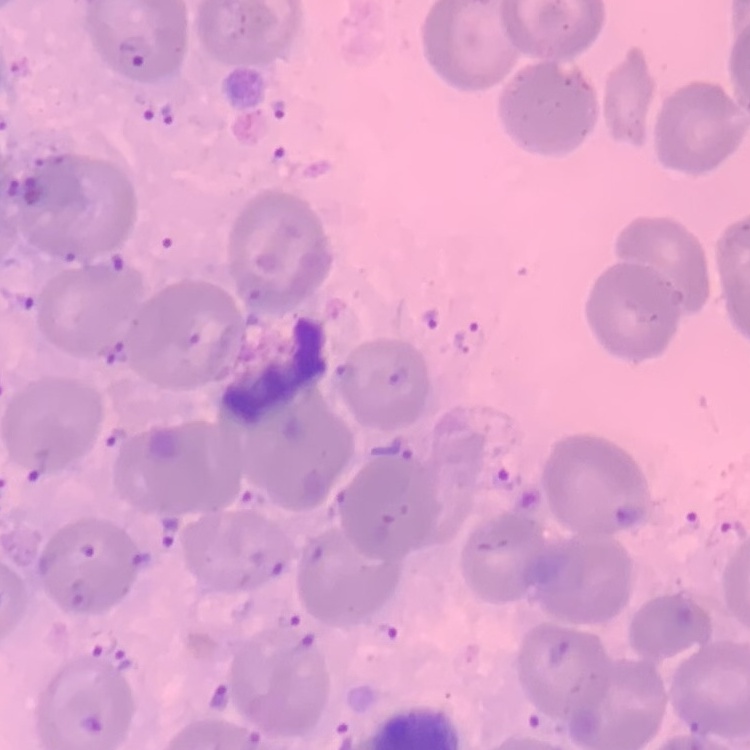

Summary:
  - Erythrocyte morphology: no rouleaux formation
  - Preparation: thin blood smear
  - Stain: Field's or Giemsa
  - Image type: square crop of a larger photomicrograph